State the blood parasite species.
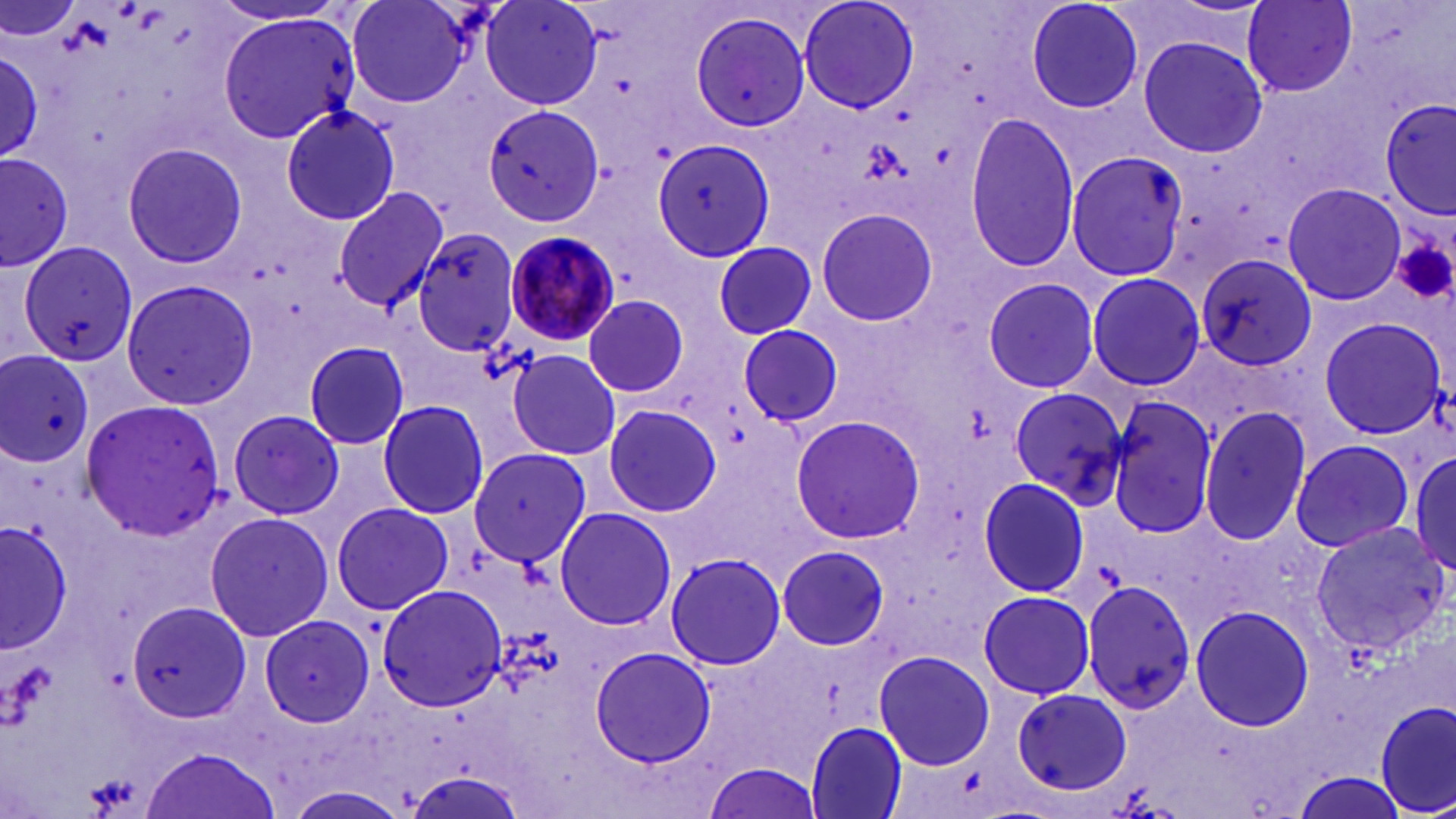

Plasmodium malariae.

Approximate bounding boxes as named x1/y1/x2/y2 corners in pixels. Plasmodium malariae-infected red blood cell locations: (x1=509, y1=235, x2=624, y2=350). Uninfected red blood cell locations: (x1=0, y1=0, x2=81, y2=47), (x1=345, y1=0, x2=477, y2=108), (x1=481, y1=0, x2=603, y2=111), (x1=798, y1=0, x2=920, y2=114), (x1=1025, y1=0, x2=1145, y2=115), (x1=1243, y1=0, x2=1359, y2=96), (x1=688, y1=10, x2=812, y2=133), (x1=215, y1=12, x2=360, y2=141), (x1=1137, y1=35, x2=1269, y2=159), (x1=0, y1=45, x2=47, y2=167), (x1=1381, y1=101, x2=1455, y2=218), (x1=482, y1=103, x2=605, y2=227), (x1=281, y1=104, x2=403, y2=227), (x1=964, y1=111, x2=1081, y2=275), (x1=651, y1=140, x2=777, y2=265), (x1=121, y1=142, x2=248, y2=269), (x1=1, y1=150, x2=74, y2=274), (x1=1066, y1=150, x2=1187, y2=280), (x1=1282, y1=183, x2=1407, y2=306), (x1=332, y1=188, x2=447, y2=312), (x1=815, y1=205, x2=940, y2=328), (x1=411, y1=226, x2=522, y2=355), (x1=714, y1=240, x2=816, y2=340), (x1=19, y1=242, x2=140, y2=368), (x1=1195, y1=253, x2=1318, y2=374), (x1=1086, y1=272, x2=1206, y2=390), (x1=981, y1=277, x2=1100, y2=392), (x1=121, y1=279, x2=258, y2=409), (x1=582, y1=295, x2=690, y2=399), (x1=1317, y1=315, x2=1449, y2=442), (x1=1320, y1=317, x2=1448, y2=439), (x1=737, y1=326, x2=847, y2=430), (x1=302, y1=340, x2=410, y2=450), (x1=507, y1=347, x2=622, y2=459), (x1=1, y1=351, x2=94, y2=465), (x1=1008, y1=384, x2=1128, y2=507), (x1=1100, y1=392, x2=1220, y2=536), (x1=80, y1=396, x2=230, y2=543), (x1=1102, y1=397, x2=1220, y2=539), (x1=377, y1=399, x2=490, y2=519), (x1=602, y1=402, x2=722, y2=517), (x1=1199, y1=404, x2=1313, y2=545), (x1=228, y1=409, x2=343, y2=520), (x1=789, y1=414, x2=925, y2=543), (x1=1289, y1=438, x2=1415, y2=553), (x1=468, y1=445, x2=591, y2=568), (x1=1410, y1=448, x2=1456, y2=573), (x1=977, y1=477, x2=1090, y2=598), (x1=331, y1=502, x2=453, y2=615), (x1=554, y1=504, x2=677, y2=631), (x1=204, y1=511, x2=333, y2=642), (x1=1, y1=518, x2=77, y2=656), (x1=1309, y1=522, x2=1449, y2=652), (x1=777, y1=546, x2=891, y2=651), (x1=666, y1=552, x2=785, y2=672), (x1=1082, y1=579, x2=1193, y2=716), (x1=376, y1=582, x2=510, y2=712), (x1=978, y1=590, x2=1094, y2=699), (x1=127, y1=599, x2=251, y2=721), (x1=1189, y1=604, x2=1315, y2=733), (x1=258, y1=615, x2=374, y2=728), (x1=589, y1=645, x2=717, y2=770), (x1=873, y1=649, x2=993, y2=772), (x1=1011, y1=687, x2=1134, y2=795), (x1=1375, y1=700, x2=1455, y2=817), (x1=806, y1=721, x2=909, y2=819), (x1=141, y1=745, x2=283, y2=819), (x1=703, y1=760, x2=824, y2=819), (x1=1292, y1=773, x2=1408, y2=817), (x1=279, y1=787, x2=410, y2=819). Platelet locations: (x1=1392, y1=238, x2=1456, y2=306). Light microscopy. May-Grünwald-Giemsa stain. Thin blood smear. One field of a larger specimen. Image is 1456×819 pixels. Captured at 1000x magnification.